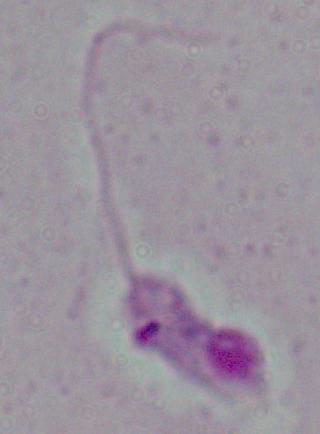

Summary:
  - Magnification: 1000x
  - Identification: Leishmania
  - Modality: photomicrograph